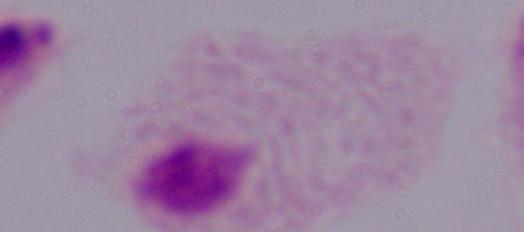

identification = trichomonad
magnification = 1000x
modality = photomicrograph